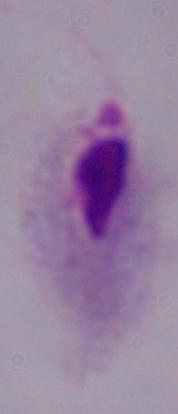
Captured at 1000x magnification. A trichomonad is seen. Micrograph.